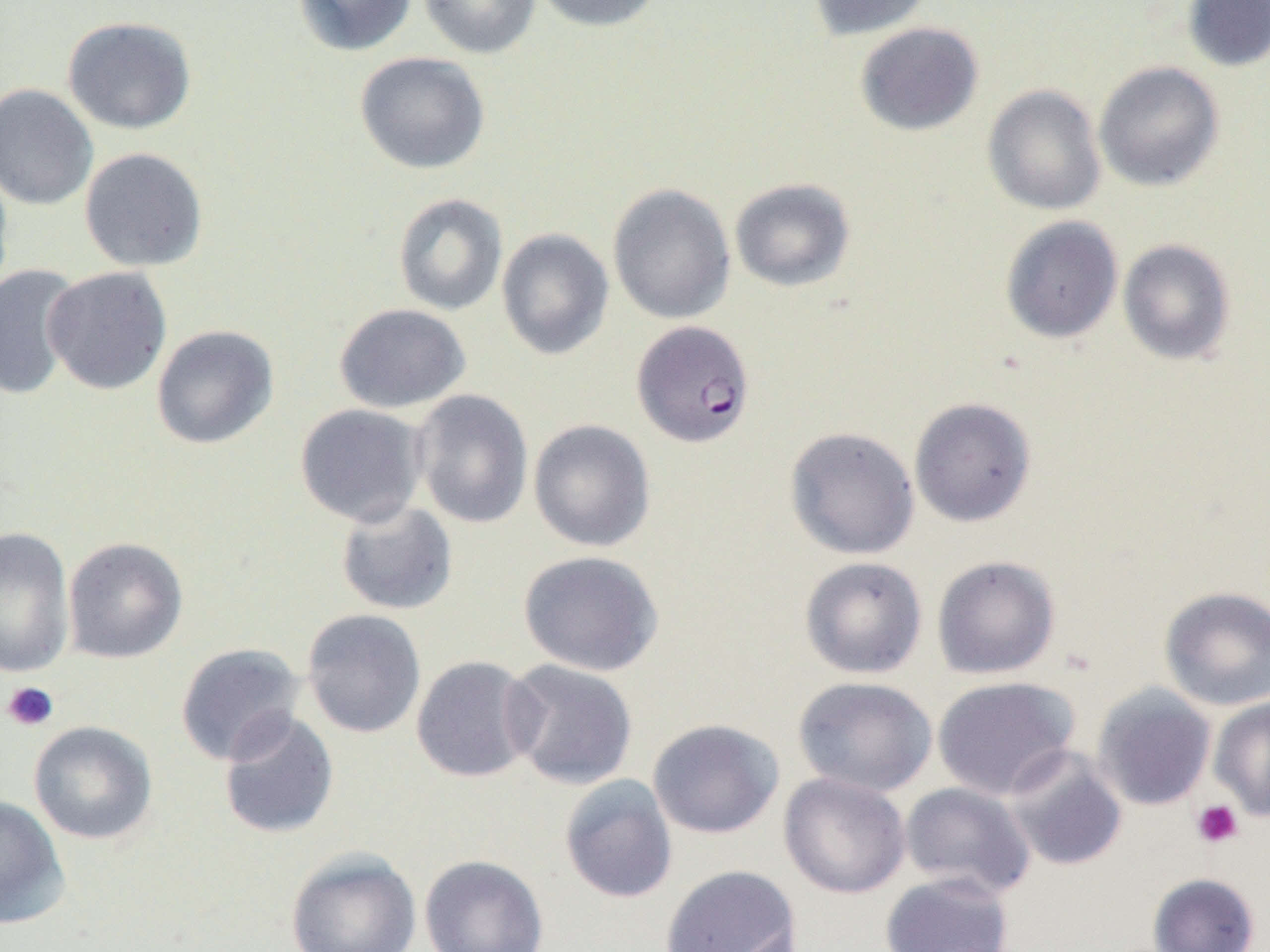
{
  "slide_level_diagnosis": "Plasmodium falciparum",
  "platelet_locations": "approximate bounding boxes as [x1, y1, x2, y2] in pixels: [2, 681, 59, 732], [1191, 799, 1244, 849]",
  "modality": "light microscopy",
  "image_size": "1270×952 pixels",
  "magnification": "1000x",
  "field_of_view": "one of a larger specimen",
  "uninfected_red_blood_cell_locations": "approximate bounding boxes as [x1, y1, x2, y2] in pixels: [292, 0, 417, 56], [418, 0, 542, 59], [531, 0, 665, 32], [806, 0, 934, 40], [1182, 0, 1270, 72], [62, 16, 197, 135], [854, 22, 984, 136], [354, 51, 490, 175], [1093, 61, 1224, 191], [0, 83, 98, 210], [982, 84, 1107, 215], [79, 147, 209, 272], [0, 160, 14, 301], [729, 178, 856, 292], [608, 183, 736, 324], [393, 193, 508, 316], [1000, 216, 1123, 344], [496, 228, 614, 360], [1117, 239, 1236, 366], [0, 264, 83, 401], [42, 266, 172, 395], [333, 303, 471, 413], [151, 324, 279, 450], [411, 389, 534, 529], [909, 397, 1036, 527], [294, 403, 429, 527], [528, 419, 656, 553], [784, 426, 920, 560], [334, 499, 459, 616], [0, 526, 76, 679], [62, 536, 189, 663], [518, 550, 664, 676], [931, 555, 1061, 679], [799, 556, 928, 679], [1158, 585, 1270, 711], [301, 608, 426, 739], [175, 642, 306, 766], [411, 655, 540, 783], [502, 659, 639, 790], [792, 676, 938, 797], [931, 676, 1080, 800], [1091, 684, 1217, 811], [1209, 695, 1270, 821], [218, 710, 339, 839], [647, 718, 784, 839], [28, 720, 158, 844], [1003, 746, 1128, 871], [778, 772, 911, 899], [559, 774, 678, 904], [899, 781, 1036, 899], [0, 795, 69, 929], [285, 848, 422, 952], [420, 854, 549, 952], [660, 864, 801, 952], [880, 872, 1015, 952], [1147, 872, 1261, 952]",
  "plasmodium_falciparum_infected_red_blood_cell_locations": "approximate bounding boxes as [x1, y1, x2, y2] in pixels: [632, 320, 755, 448]",
  "preparation": "thin blood film"
}